Assess this cell for malaria.
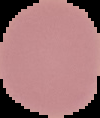

Uninfected.

Segmented cell region on a black background. From a thin blood film. Image is 100×118 pixels.